Locate every Plasmodium parasite.
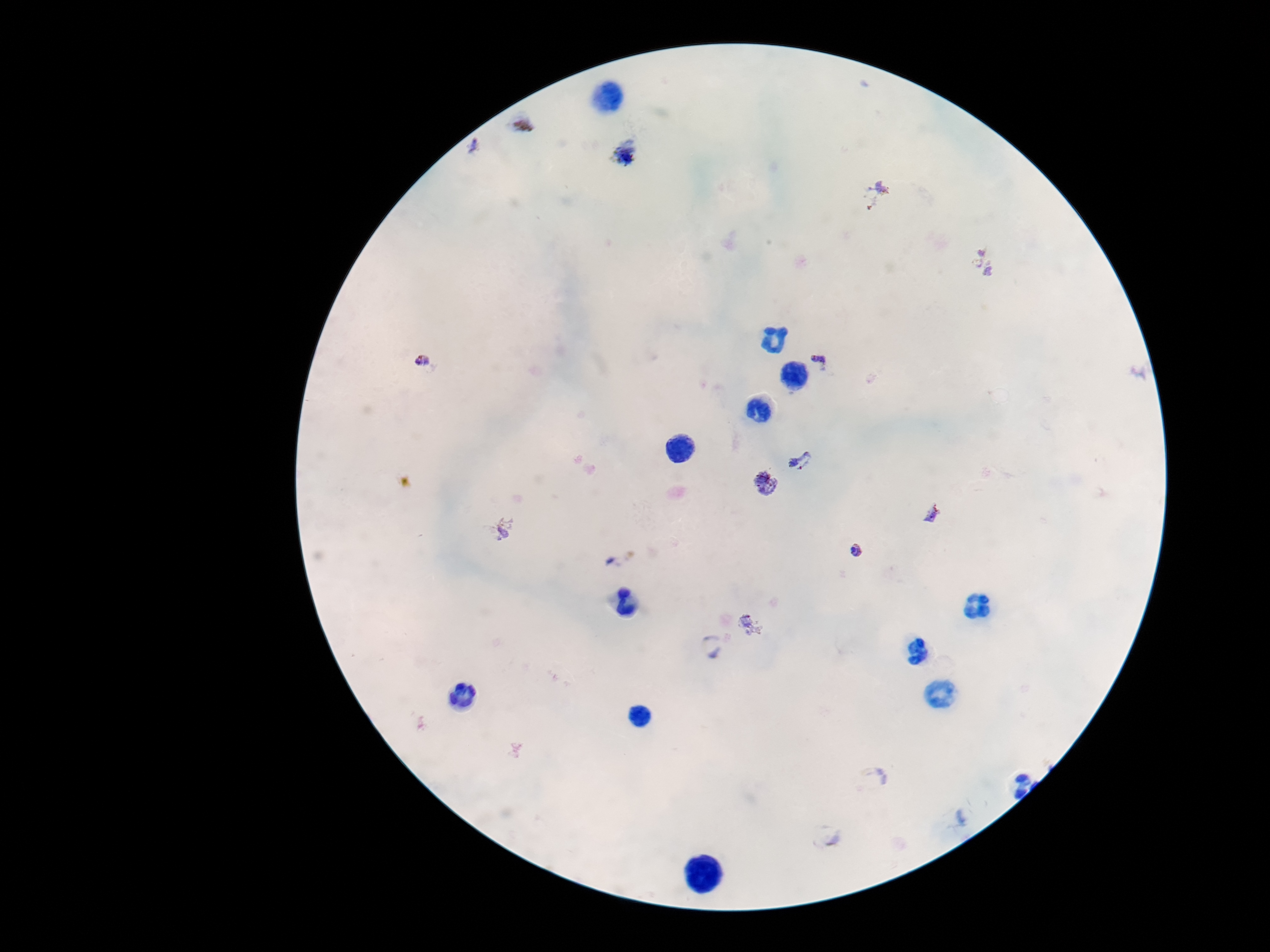

Approximate object centers, in pixels from the top-left corner.
Plasmodium parasites: (x=523, y=124), (x=474, y=146), (x=627, y=153), (x=877, y=193), (x=984, y=263), (x=821, y=359), (x=423, y=362), (x=802, y=460), (x=765, y=483), (x=932, y=513), (x=501, y=529), (x=858, y=550), (x=625, y=560), (x=752, y=625), (x=710, y=647), (x=874, y=778), (x=825, y=836).

Image is 1270×952 pixels. One field from this slide. Thick blood film. Patient malaria status: infected. Giemsa-stained preparation. 100x magnification. Photographed through the microscope eyepiece with a smartphone camera.